Assess this cell for malaria.
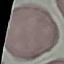
Uninfected.

capture = smartphone camera at the microscope eyepiece
image type = automatically extracted cell patch, resized to 64 × 64 pixels
preparation = thin blood smear
stain = Giemsa